State the preparation type.
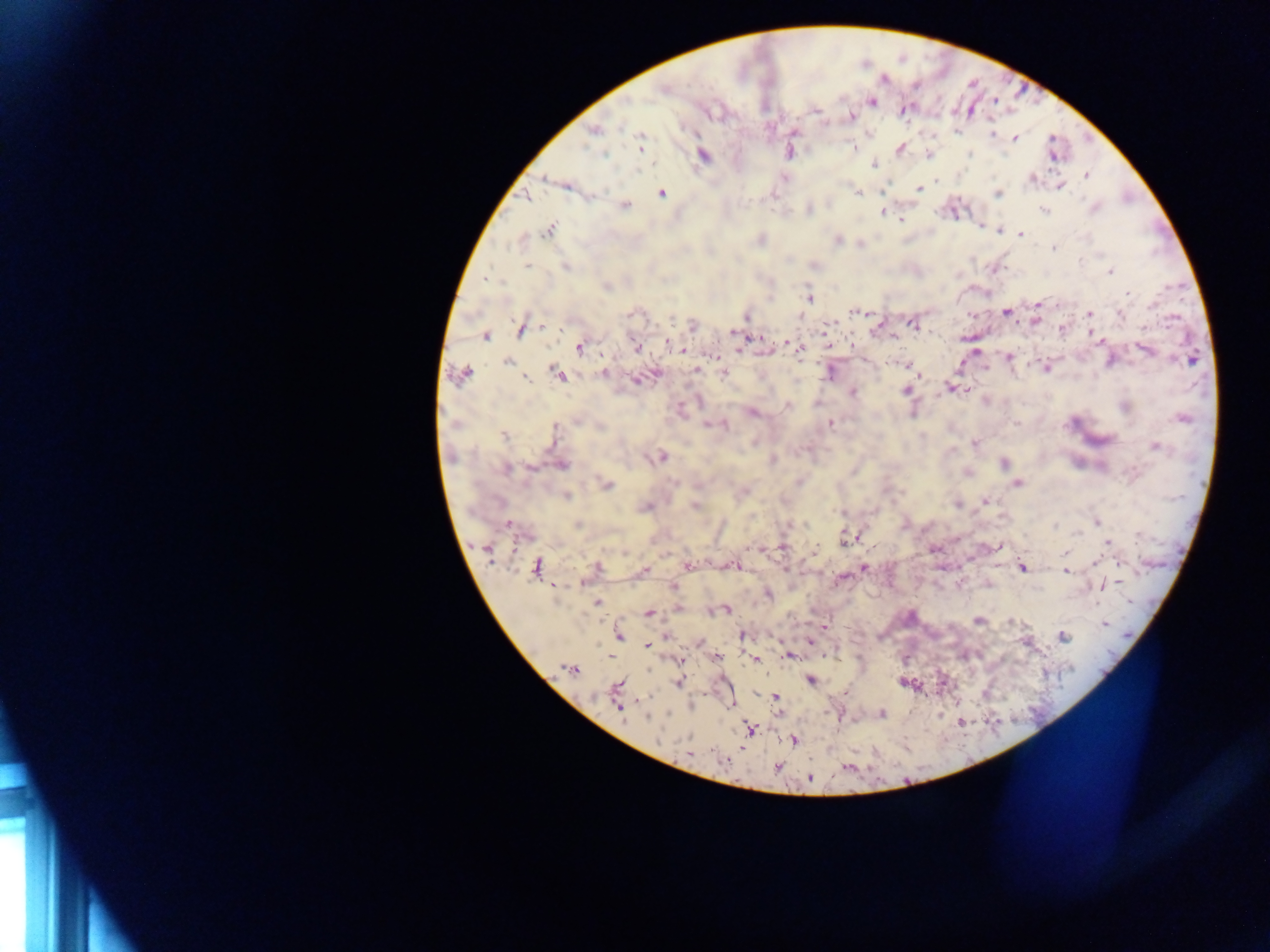

Thick blood smear.

Approximate centers as [x, y] in pixels.
Summary:
  - Plasmodium parasite locations: [663, 89], [872, 101], [815, 111], [850, 116], [594, 130], [991, 133], [1014, 138], [641, 144], [854, 147], [900, 149], [789, 153], [971, 153], [604, 154], [703, 156], [874, 164], [1086, 175], [544, 178], [1033, 179], [935, 180], [568, 187], [1061, 187], [918, 189], [858, 192], [662, 193], [998, 193], [525, 197], [625, 206], [1094, 208], [1044, 209], [883, 212], [886, 214], [901, 219], [981, 227], [548, 229], [1020, 235], [761, 239], [837, 240], [1054, 248], [527, 266], [566, 267], [994, 270], [1110, 272], [485, 278], [606, 287], [1127, 294], [809, 298], [1039, 304], [855, 312], [1006, 313], [632, 314], [1121, 314], [1090, 315], [747, 317], [671, 318], [1037, 319], [913, 324], [543, 326], [693, 326], [1062, 328], [520, 330], [734, 332], [486, 336], [1096, 336], [892, 337], [964, 338], [667, 343], [789, 344], [636, 347], [794, 347], [579, 348], [740, 349], [799, 350], [1146, 351], [1009, 357], [1191, 360], [507, 362], [908, 365], [1045, 367], [696, 370], [603, 373], [557, 374], [828, 374], [462, 375], [723, 375], [920, 375], [527, 379], [637, 380], [950, 389], [906, 390], [965, 390], [853, 393], [787, 406], [752, 412], [1182, 418], [576, 420], [831, 423], [455, 424], [706, 425], [600, 427], [725, 427], [554, 431], [504, 436], [974, 444], [1156, 446], [661, 457], [772, 460], [1004, 464], [562, 465], [530, 468], [506, 469], [1018, 483], [607, 484], [567, 497], [986, 501], [957, 505], [695, 506], [646, 507], [1097, 522], [578, 524], [805, 524], [508, 525], [1055, 526], [1078, 533], [848, 538], [1108, 542], [782, 547], [999, 547], [815, 549], [487, 550], [1065, 553], [1096, 563], [1119, 564], [687, 565], [735, 566], [536, 567], [597, 568], [864, 568], [1022, 568], [644, 570], [1067, 571], [673, 586], [1103, 586], [768, 593], [598, 602], [678, 608], [726, 610], [649, 613], [979, 620], [1012, 621], [1104, 624], [825, 626], [742, 635], [619, 636], [666, 636], [1063, 636], [809, 643], [647, 646], [788, 656], [717, 657], [756, 660], [680, 661], [570, 668], [810, 680], [678, 683], [617, 687], [776, 696], [619, 707], [882, 714], [647, 717], [749, 729], [793, 740], [689, 753], [724, 761], [777, 767], [847, 768], [810, 778]
  - Field of view: single
  - Capture: mobile-phone photograph through a microscope
  - Country: Ghana
  - Image size: 1270×952 pixels